Describe the morphology of the red blood cells.
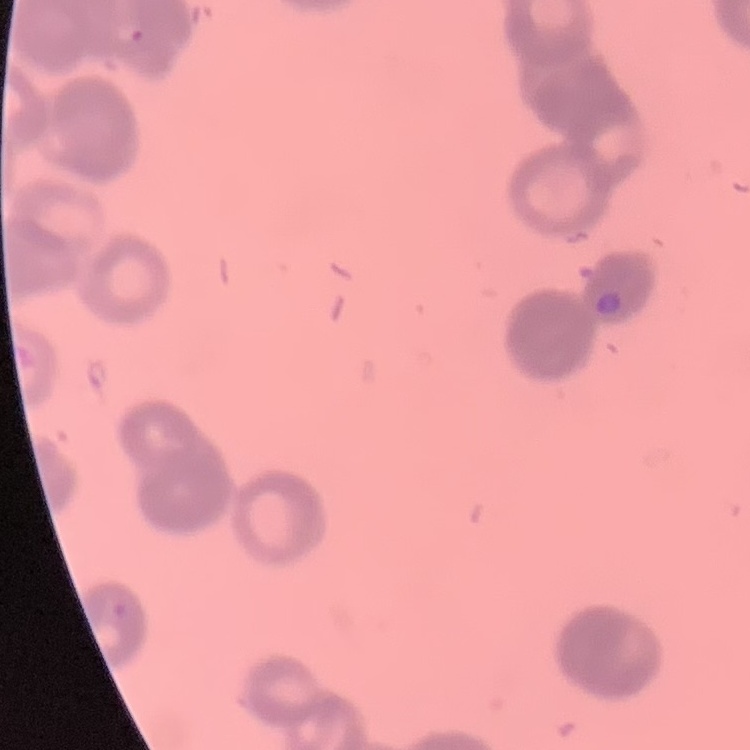

They show rouleaux formation.

Stained with either Field's or Giemsa. One tile cut from a larger photomicrograph. Thin peripheral smear.